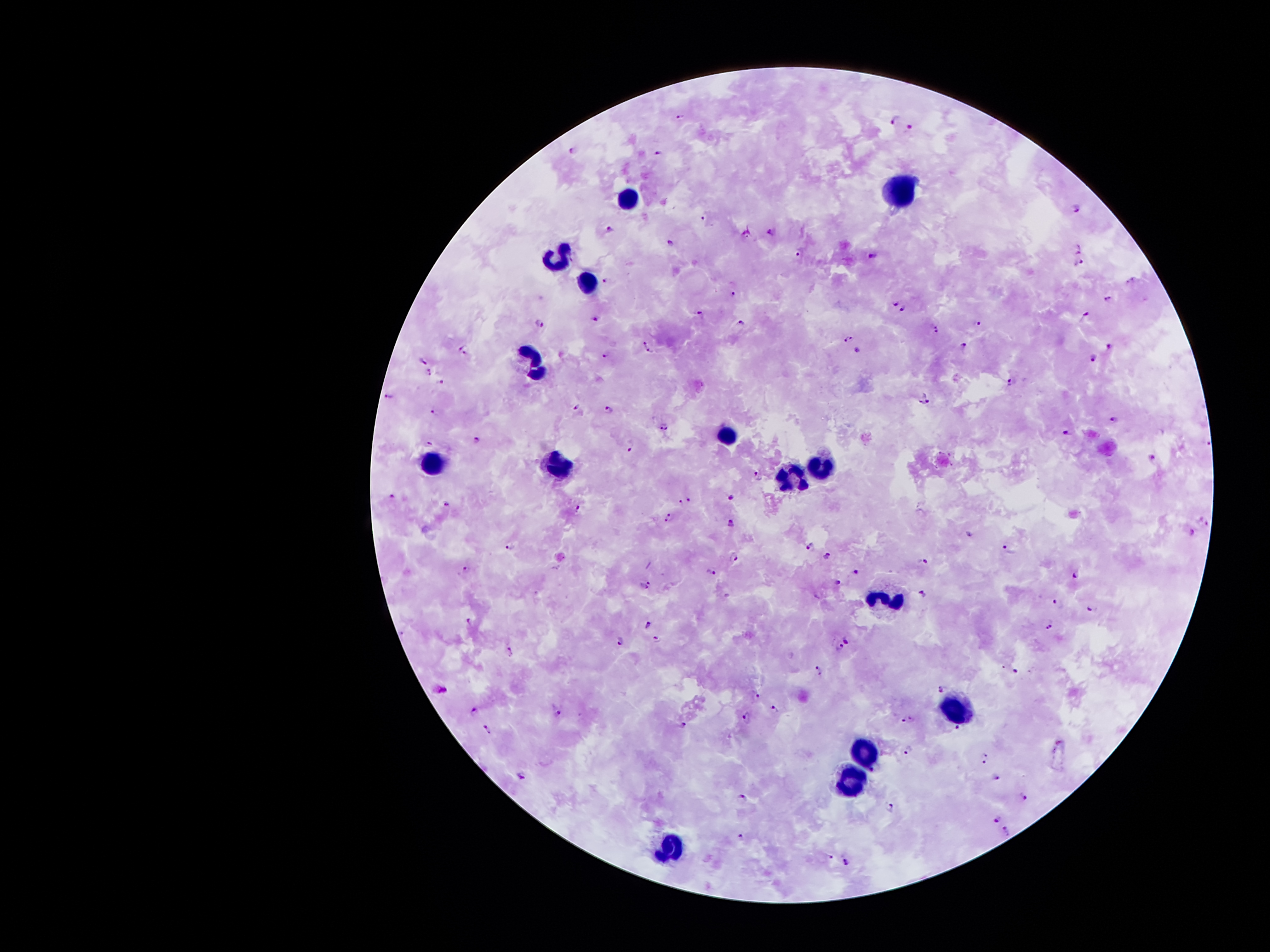
coordinate format = approximate centers as [x, y] in pixels
leukocyte locations = [901, 188], [629, 197], [558, 254], [587, 280], [534, 360], [729, 433], [435, 461], [560, 465], [820, 466], [791, 475], [887, 597], [955, 704], [869, 753], [850, 781], [667, 845]
malaria parasite locations = [681, 115], [897, 119], [911, 127], [571, 149], [658, 153], [1076, 206], [705, 218], [610, 228], [771, 231], [668, 245], [1079, 248], [799, 253], [871, 256], [1080, 263], [606, 282], [1131, 282], [734, 293], [1110, 298], [896, 301], [904, 308], [698, 312], [598, 317], [1086, 317], [741, 323], [978, 323], [539, 324], [935, 329], [849, 338], [645, 341], [965, 345], [1110, 347], [463, 349], [859, 350], [651, 353], [604, 356], [1094, 359], [422, 362], [430, 371], [443, 381], [1011, 381], [389, 396], [926, 399], [576, 406], [610, 408], [435, 410], [1114, 418], [664, 427], [1066, 434], [477, 438], [429, 442], [1208, 442], [631, 448], [1153, 458], [760, 477], [393, 498], [731, 498], [681, 501], [690, 501], [447, 503], [579, 506], [669, 517], [1205, 523], [731, 524], [1193, 531], [968, 532], [510, 546], [810, 546], [1009, 550], [827, 555], [734, 557], [921, 562], [466, 568], [856, 571], [711, 572], [1074, 575], [837, 583], [649, 584], [921, 593], [1055, 601], [1092, 609], [470, 619], [647, 624], [1050, 627], [657, 638], [848, 641], [621, 642], [840, 646], [511, 652], [820, 670], [1015, 670], [941, 688], [441, 689], [757, 696], [474, 710], [556, 710], [776, 710], [748, 716], [912, 718], [904, 721], [684, 726], [958, 726], [487, 728], [907, 750], [986, 758], [522, 776], [996, 777], [1025, 797], [743, 798], [891, 805], [997, 819], [1008, 832], [741, 836], [830, 857], [847, 863]
magnification = 100x
image size = 1270×952 pixels
stain = Giemsa
capture = smartphone camera through the microscope eyepiece
patient malaria status = positive for Plasmodium falciparum
field of view = one from this slide
preparation = thick blood film